Assess for Plasmodium parasites.
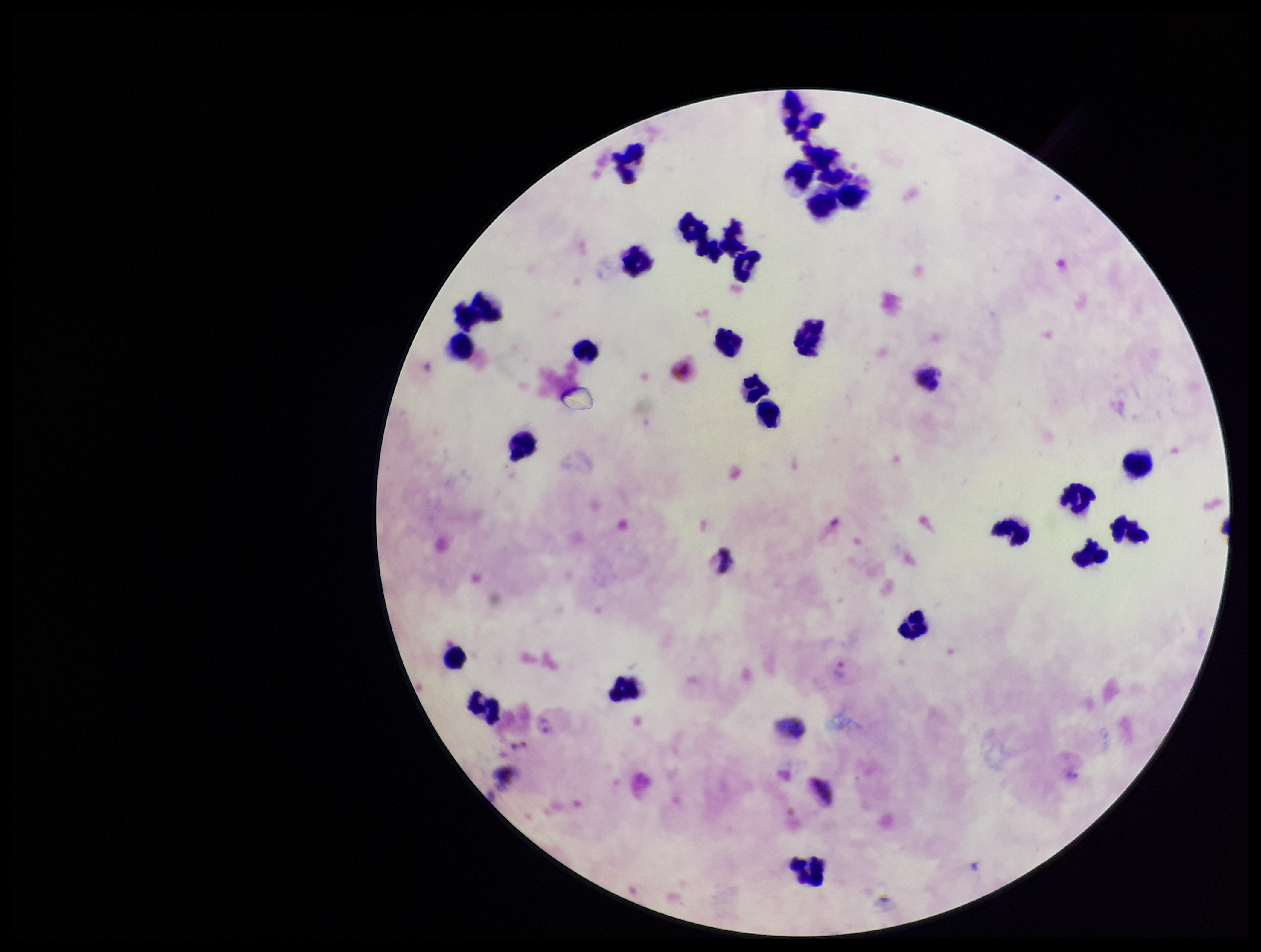

Identified.

Summary:
  - Species reported for this patient: Plasmodium vivax
  - Preparation: thick blood smear
  - Leukocyte count: 28
  - Image size: 1261×952 pixels
  - Parasite count: 2
  - Stain: Giemsa
  - Capture: smartphone photograph through the microscope eyepiece
  - Patient malaria status: positive
  - Field of view: one from this slide